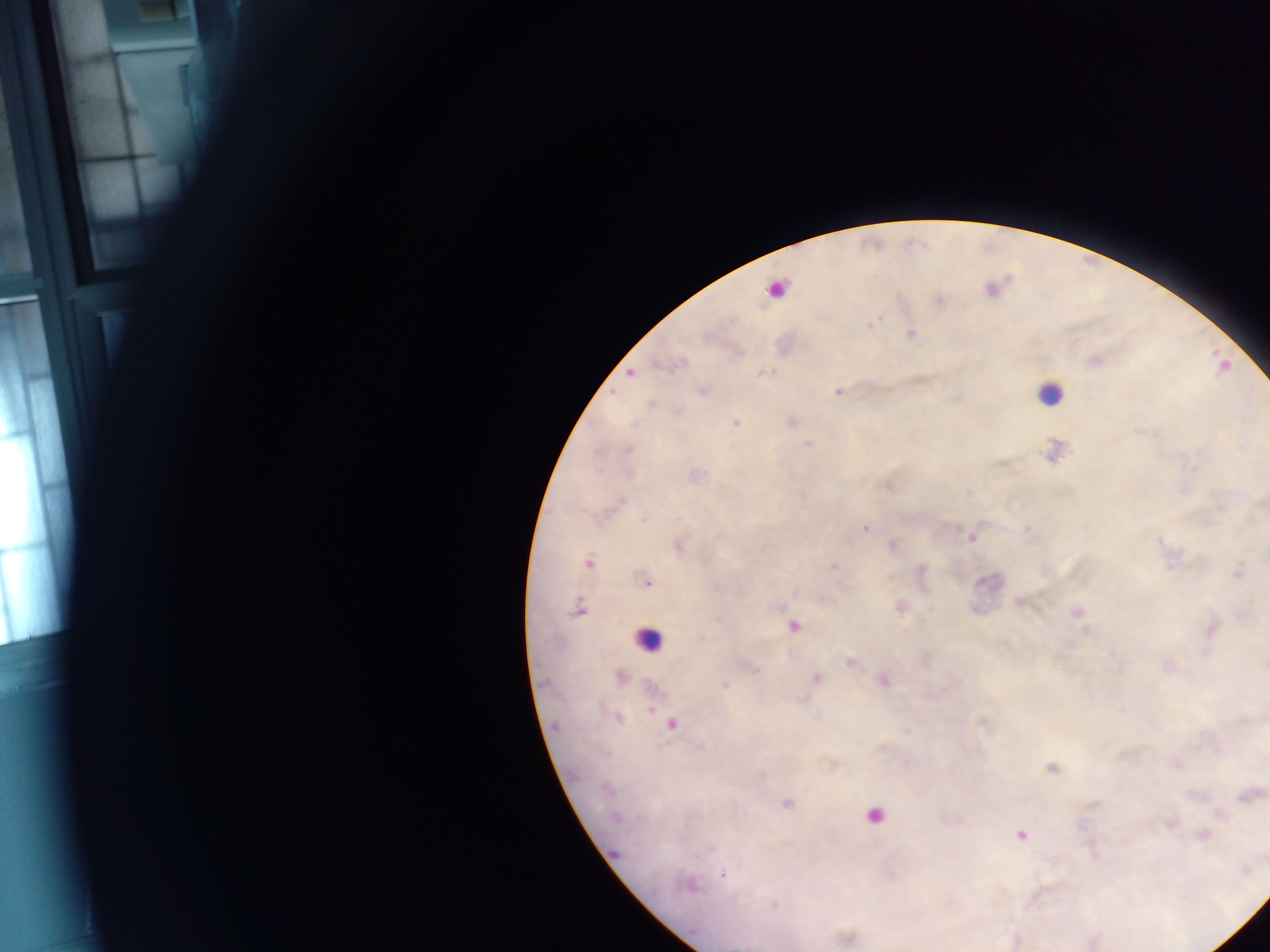

Approximate centers as [x, y] in pixels. Leukocyte locations: [774, 289], [1050, 394], [648, 638], [874, 818]. Plasmodium parasite locations: [871, 325], [910, 334], [631, 373], [763, 373], [702, 390], [838, 391], [651, 405], [735, 423], [807, 444], [621, 501], [864, 528], [971, 538], [678, 545], [893, 545], [588, 563], [833, 567], [1239, 573], [646, 582], [579, 610], [1078, 612], [792, 626], [1264, 665], [753, 668], [620, 676], [816, 677], [884, 682], [725, 685], [651, 710], [619, 718], [671, 724], [1051, 768], [762, 775], [1248, 796], [787, 804], [1204, 834], [1020, 835], [723, 874], [692, 887], [774, 904]. Mobile-phone photograph taken through the microscope. Single field of view. Collected in Ghana. Thick blood film. Image is 1270×952 pixels.